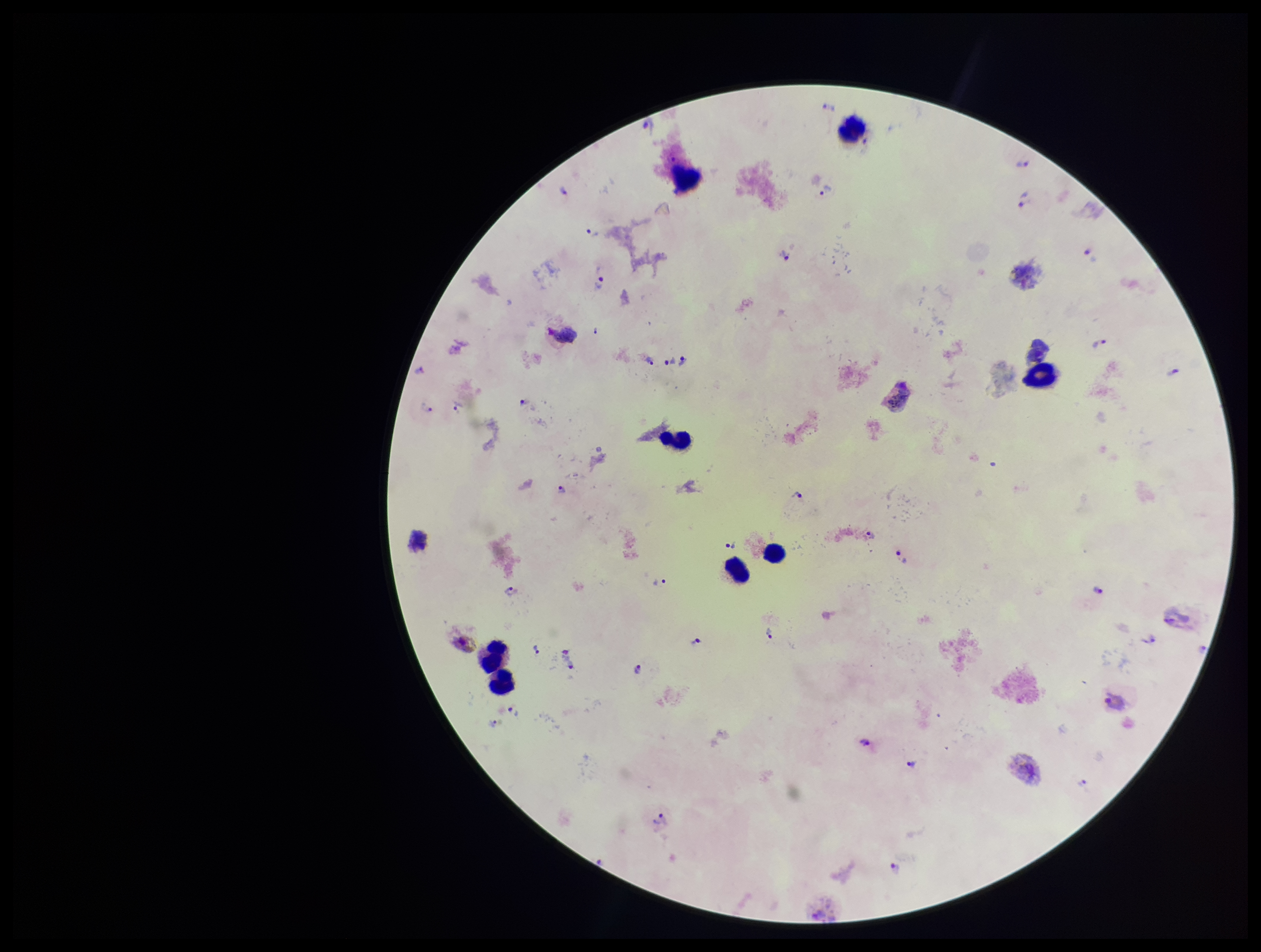
{
  "species_reported_for_this_patient": "Plasmodium vivax",
  "capture": "smartphone photograph through the microscope eyepiece",
  "leukocyte_count": 8,
  "field_of_view": "single",
  "parasite_count": 32,
  "patient_malaria_status": "infected",
  "image_size": "1261×952 pixels",
  "stain": "Giemsa",
  "preparation": "thick smear",
  "plasmodium_parasites": "identified"
}